State which cell type is depicted.
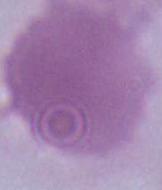

This is an erythrocyte.

magnification = 1000x
modality = micrograph